Assess this cell for malaria.
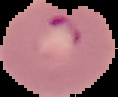

It is parasitized.

preparation = thin blood smear
image size = 118×97 pixels
image type = segmented cell region on a black background